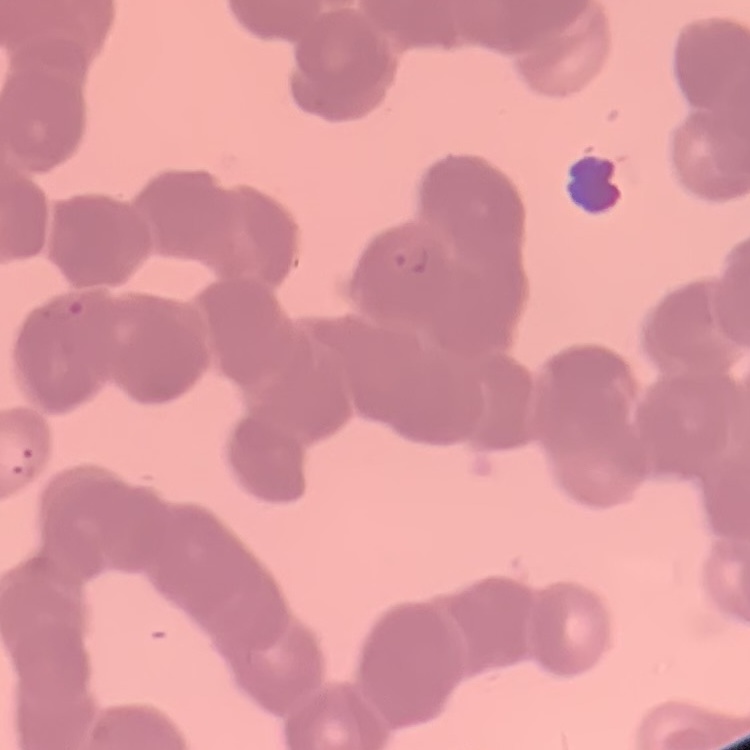

red blood cell morphology = rouleaux formation
image type = one tile cut from a larger photomicrograph
stain = Field's or Giemsa
preparation = thin blood film